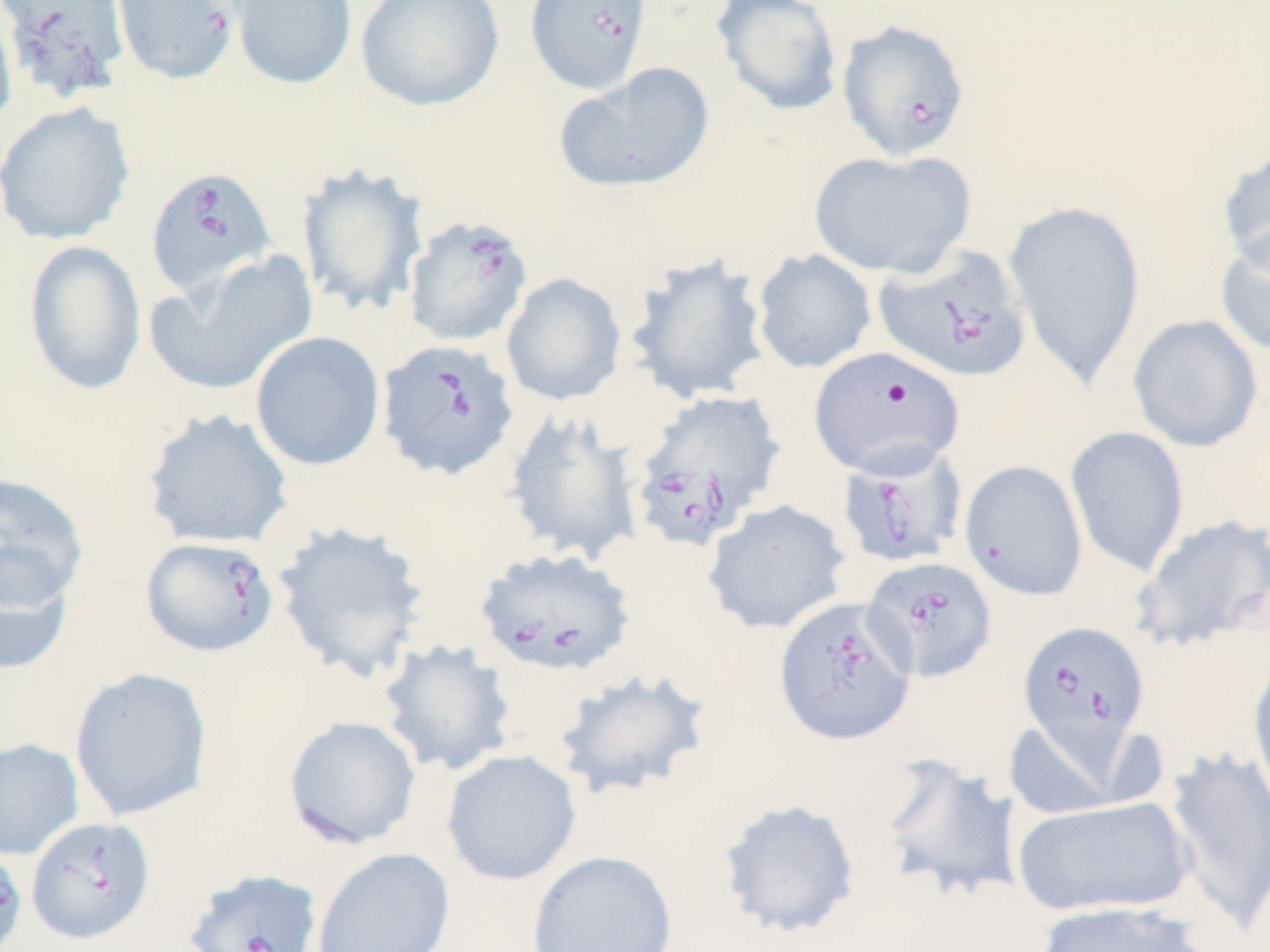

slide-level diagnosis = Babesia divergens
preparation = thin blood smear
Babesia divergens-infected red blood cell locations = approximate bounding boxes as (x1,y1)-(x2,y2) corner pairs in pixels: (111,0)-(241,85), (524,0)-(653,95), (837,19)-(971,163), (145,165)-(278,300), (403,214)-(534,347), (873,245)-(1032,383), (375,338)-(519,482), (627,389)-(787,550), (837,444)-(969,570), (140,535)-(280,658), (474,546)-(636,678), (861,556)-(997,683), (773,597)-(917,746), (1017,620)-(1149,758), (26,816)-(155,944), (0,845)-(28,951), (183,868)-(323,952)
stain = May-Grünwald-Giemsa
modality = optical microscopy
uninfected red blood cell locations = approximate bounding boxes as (x1,y1)-(x2,y2) corner pairs in pixels: (227,0)-(358,91), (354,0)-(506,112), (711,0)-(844,117), (0,1)-(18,140), (1,1)-(131,103), (554,63)-(714,194), (1,101)-(135,245), (1218,142)-(1270,274), (808,148)-(976,279), (296,162)-(429,319), (1004,199)-(1146,387), (1215,224)-(1270,357), (23,239)-(146,396), (752,249)-(877,374), (145,252)-(318,398), (624,253)-(772,406), (501,273)-(627,406), (1128,314)-(1264,453), (250,331)-(385,472), (804,346)-(960,480), (141,408)-(294,550), (502,409)-(643,566), (1064,426)-(1189,578), (959,460)-(1088,600), (0,472)-(89,609), (702,499)-(852,635), (1131,513)-(1270,653), (270,520)-(432,683), (0,551)-(74,677), (375,639)-(516,778), (1246,657)-(1270,808), (72,665)-(217,820), (552,667)-(714,802), (1002,717)-(1131,821), (286,719)-(424,844), (0,738)-(84,860), (1164,745)-(1270,935), (441,749)-(582,886), (871,751)-(1023,905), (1013,795)-(1194,918), (716,797)-(861,940), (311,847)-(454,952), (526,849)-(678,952), (1036,900)-(1208,952)
image size = 1270×952 pixels
magnification = 1000x
field of view = single